Name the blood parasite species.
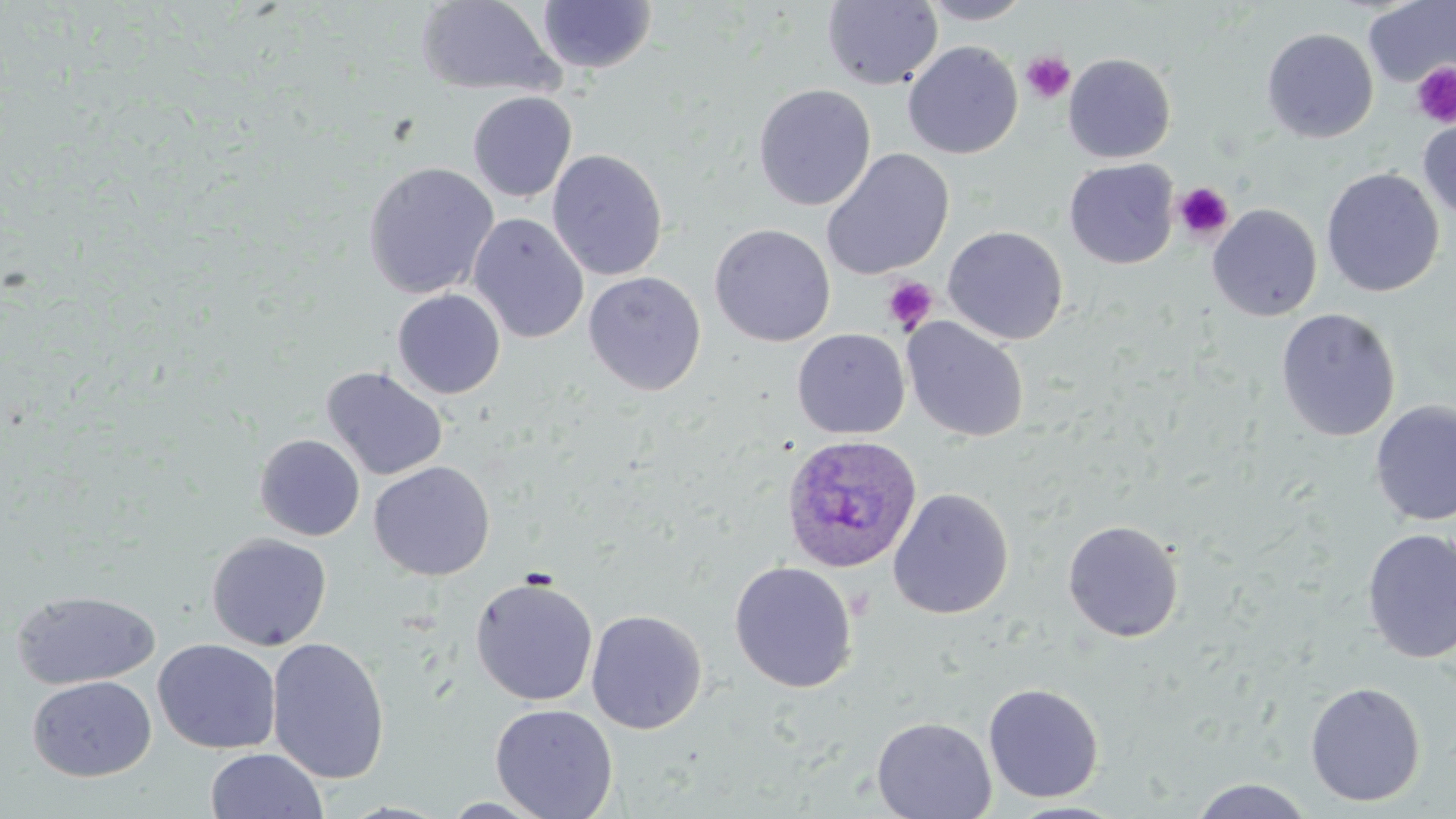

Plasmodium ovale.

Summary:
  - Coordinate format: approximate bounding boxes as (x1,y1)-(x2,y2) corner pairs in pixels
  - Platelet locations: (1021,51)-(1076,104), (1411,62)-(1456,128), (1173,181)-(1234,242), (882,276)-(938,334)
  - Plasmodium ovale-infected red blood cell locations: (781,434)-(924,575)
  - Uninfected red blood cell locations: (920,0)-(1034,25), (417,1)-(562,98), (536,1)-(657,74), (822,1)-(943,89), (1364,1)-(1456,88), (1261,28)-(1378,143), (902,41)-(1023,159), (1063,53)-(1176,163), (753,83)-(876,211), (467,92)-(577,202), (1418,115)-(1456,223), (821,148)-(955,280), (547,149)-(668,281), (1064,159)-(1179,269), (362,161)-(500,300), (1321,168)-(1444,297), (1208,204)-(1322,321), (467,213)-(590,344), (709,223)-(836,347), (942,225)-(1068,344), (583,271)-(706,396), (392,289)-(506,399), (1276,308)-(1401,442), (901,317)-(1029,443), (791,328)-(910,439), (321,365)-(448,481), (1370,401)-(1456,527), (255,434)-(364,541), (368,461)-(496,580), (888,487)-(1014,619), (1062,519)-(1184,642), (1361,528)-(1456,664), (206,533)-(332,651), (729,561)-(858,693), (470,575)-(599,706), (10,589)-(161,690), (585,608)-(708,734), (267,636)-(391,784), (153,638)-(281,754), (27,675)-(156,782), (1305,681)-(1426,806), (983,682)-(1104,803), (490,703)-(618,819), (871,716)-(997,818), (205,748)-(328,819), (1187,778)-(1317,818), (438,796)-(552,818), (1003,800)-(1130,819)
  - Magnification: 1000x
  - Field of view: single
  - Stain: May-Grünwald-Giemsa
  - Image size: 1456×819 pixels
  - Preparation: thin blood film
  - Modality: optical microscopy